Report the malaria status of this cell.
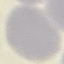
It is uninfected.

capture = smartphone camera at the microscope eyepiece
stain = Giemsa
image type = automatically extracted cell patch, resized to 64 × 64 pixels
preparation = thin blood smear